Identify the parasite.
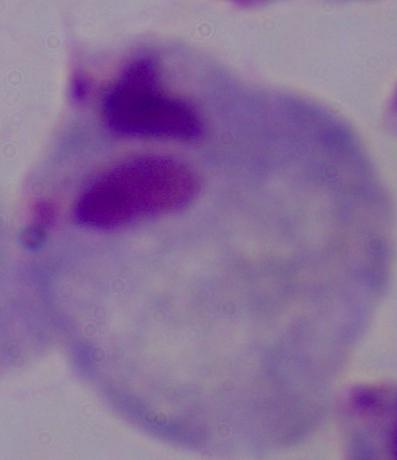

This is a trichomonad.

Photomicrograph. 1000x magnification.